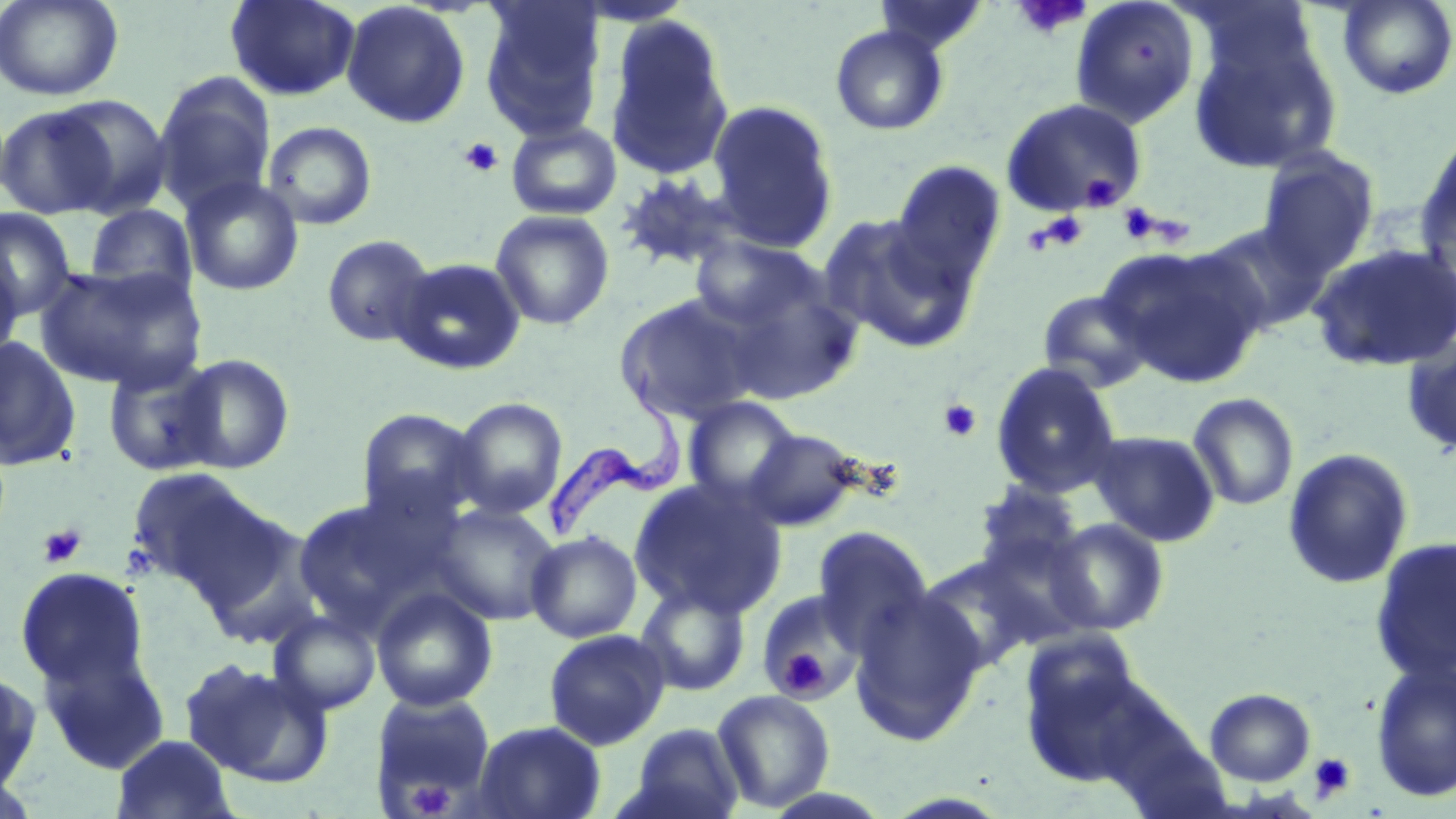
slide-level diagnosis = Trypanosoma brucei
preparation = thin blood smear
magnification = 1000x
Trypanosoma brucei locations = approximate bounding boxes as (x1, y1, x2, y2) in pixels: (546, 353, 687, 546)
image size = 1456×819 pixels
uninfected red blood cell locations (subset) = approximate bounding boxes as (x1, y1, x2, y2) in pixels: (0, 0, 124, 101), (224, 0, 361, 101), (478, 0, 606, 142), (873, 0, 990, 56), (1070, 0, 1200, 130), (1337, 0, 1456, 100), (341, 1, 471, 128), (603, 17, 735, 181), (830, 25, 949, 136), (1187, 29, 1342, 175), (153, 72, 276, 215), (51, 95, 173, 217), (706, 100, 839, 252), (0, 104, 118, 219), (506, 120, 622, 220), (262, 122, 378, 230), (1416, 129, 1456, 273), (1257, 149, 1379, 274), (890, 160, 1007, 291), (615, 172, 754, 275), (181, 175, 304, 296), (84, 204, 197, 301), (1, 208, 76, 322), (490, 209, 615, 330), (819, 214, 980, 354), (1198, 219, 1334, 335), (321, 234, 436, 348), (690, 235, 828, 333), (1307, 242, 1456, 373), (1103, 245, 1267, 387), (0, 252, 23, 367), (392, 257, 526, 375), (36, 264, 205, 391), (719, 277, 862, 405), (1037, 289, 1155, 393), (613, 293, 764, 425), (0, 335, 81, 472), (1402, 338, 1456, 457), (172, 353, 295, 474), (103, 356, 224, 476), (989, 361, 1123, 499), (1187, 392, 1299, 511), (449, 397, 568, 519), (682, 397, 800, 505), (355, 408, 484, 526), (742, 427, 865, 532), (1087, 430, 1220, 546), (1281, 448, 1414, 591), (125, 467, 272, 596), (628, 477, 787, 619), (974, 481, 1084, 577), (292, 495, 435, 632), (431, 502, 562, 625), (1044, 518, 1170, 636), (811, 527, 934, 656), (525, 530, 642, 643), (1369, 536, 1456, 684), (14, 566, 151, 695), (635, 582, 751, 696), (371, 586, 498, 712), (757, 589, 867, 705), (849, 589, 986, 745), (269, 611, 381, 715), (543, 629, 671, 751), (34, 633, 171, 776), (1018, 639, 1164, 790), (179, 658, 333, 788), (1371, 661, 1456, 803), (0, 665, 41, 795), (1204, 688, 1316, 786), (712, 690, 835, 812), (372, 691, 497, 806), (472, 720, 606, 819), (624, 722, 746, 819), (111, 734, 238, 819), (0, 773, 46, 818)
stain = May-Grünwald-Giemsa
field of view = single
platelet locations (subset) = approximate bounding boxes as (x1, y1, x2, y2) in pixels: (1011, 0, 1092, 39), (458, 136, 504, 177), (1079, 171, 1123, 211), (1117, 203, 1161, 243), (1033, 211, 1089, 253), (938, 399, 983, 443), (38, 524, 86, 568), (779, 653, 828, 698), (1309, 752, 1356, 802), (410, 780, 455, 817)
modality = optical microscopy